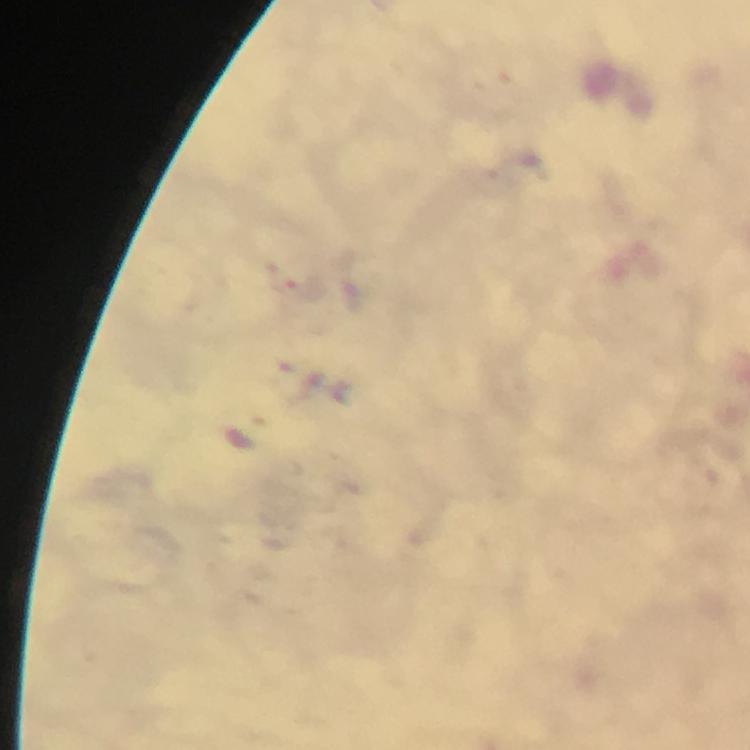

immersion oil = used
context = from a malaria diagnostic workup
capture = smartphone photograph through a microscope
stain = Giemsa
image size = 750×750 pixels
Plasmodium parasite locations = approximate centers as (x, y) in pixels: (306, 292)
magnification = 100x
preparation = thick blood smear
cropped from = a single field of view